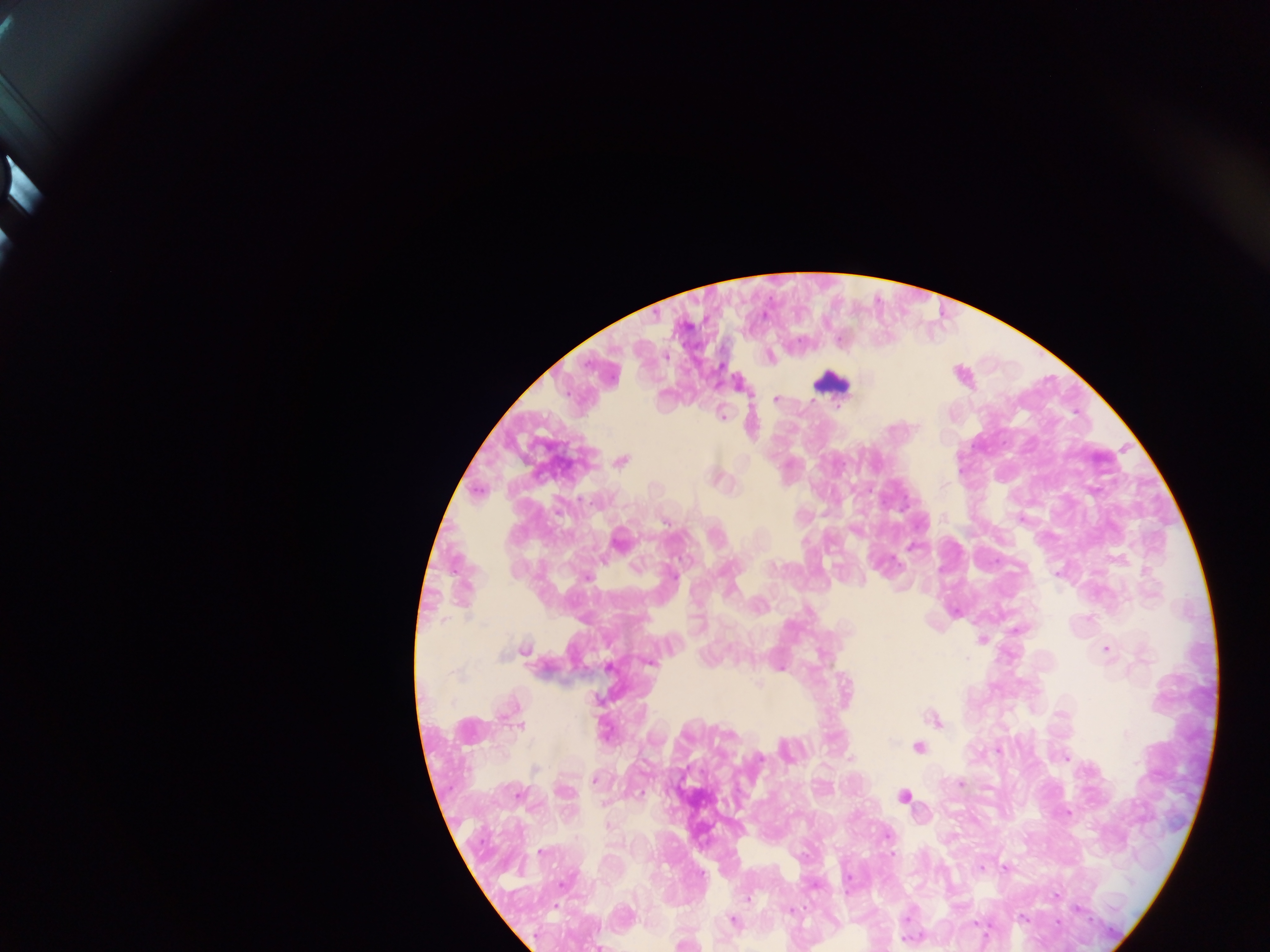
Approximate centers as [x, y] in pixels.
Summary:
  - Leukocyte locations: [833, 380]
  - Plasmodium parasite locations: [771, 356], [964, 373], [779, 399], [723, 412], [623, 458], [791, 466], [721, 475], [479, 489], [1024, 516], [621, 536], [915, 546], [1148, 568], [957, 608], [1089, 617], [1019, 629], [984, 638], [526, 648], [1107, 648], [610, 666], [781, 666], [760, 684], [599, 698], [936, 717], [522, 725], [920, 746], [1067, 757], [595, 778], [962, 781], [906, 794], [608, 803], [1067, 811], [610, 824], [543, 850], [1007, 866], [981, 867], [1057, 895], [558, 906], [792, 909], [1024, 918], [736, 919], [687, 941], [601, 946]
  - Preparation: thick blood film
  - Field of view: single
  - Capture: mobile-phone photograph through a microscope
  - Country: Ghana
  - Image size: 1270×952 pixels